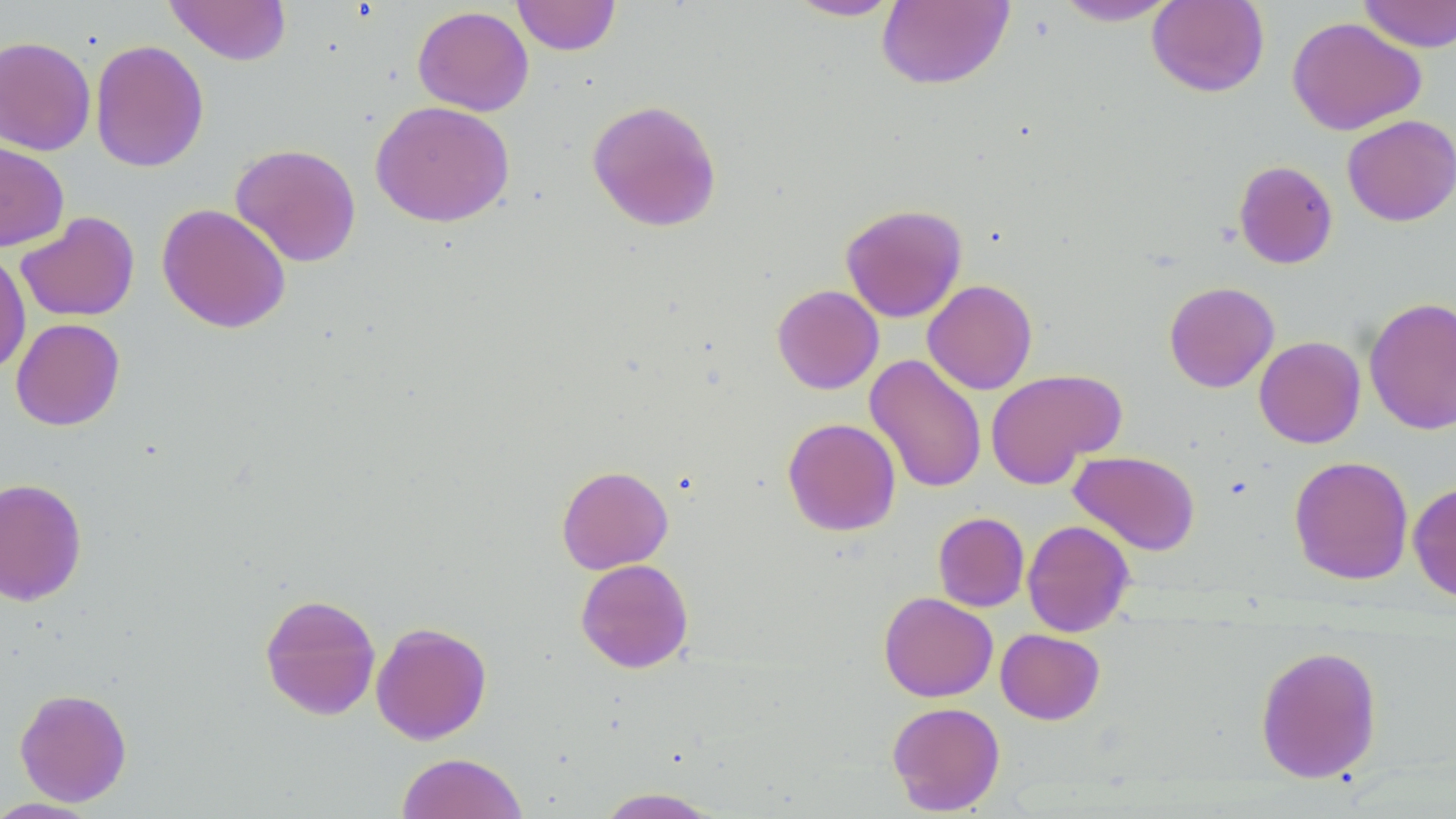
slide-level diagnosis = negative for blood parasites
magnification = 1000x
modality = optical microscopy
uninfected red blood cell locations = approximate bounding boxes as (x1,y1)-(x2,y2) corner pairs in pixels: (164,0)-(292,65), (512,0)-(620,55), (784,0)-(904,21), (1051,0)-(1182,26), (1146,0)-(1270,97), (1358,0)-(1456,53), (877,1)-(1015,92), (412,5)-(534,116), (1287,16)-(1426,136), (0,35)-(96,156), (90,40)-(210,173), (586,99)-(722,232), (370,101)-(515,227), (1342,115)-(1456,226), (0,141)-(69,251), (230,143)-(362,268), (1233,160)-(1338,269), (157,203)-(291,334), (840,203)-(967,323), (15,212)-(140,322), (0,248)-(31,376), (922,279)-(1037,395), (1164,281)-(1279,393), (772,284)-(884,394), (1364,296)-(1456,435), (11,318)-(125,431), (1254,336)-(1365,448), (864,354)-(987,494), (985,368)-(1126,488), (782,417)-(901,536), (1069,450)-(1201,556), (1289,455)-(1414,585), (556,464)-(673,574), (0,477)-(87,606), (1408,481)-(1456,603), (933,512)-(1029,612), (1022,519)-(1135,637), (575,558)-(694,673), (879,592)-(998,702), (259,593)-(381,720), (370,621)-(492,745), (995,628)-(1105,724), (1255,644)-(1382,783), (14,688)-(132,806), (887,701)-(1005,815), (396,753)-(529,818), (594,788)-(724,818), (0,797)-(101,818)
stain = May-Grünwald-Giemsa
field of view = single
image size = 1456×819 pixels
preparation = thin blood smear